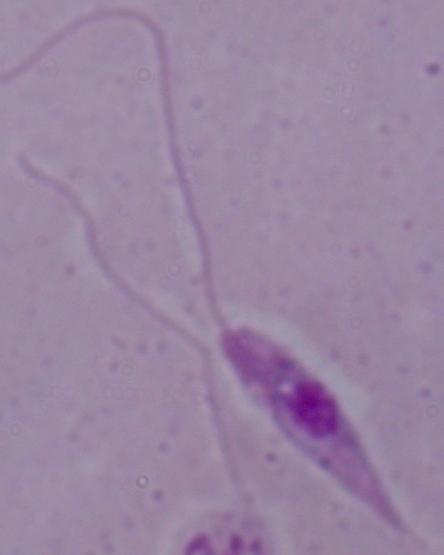

{
  "magnification": "1000x",
  "identification": "Leishmania",
  "modality": "photomicrograph"
}